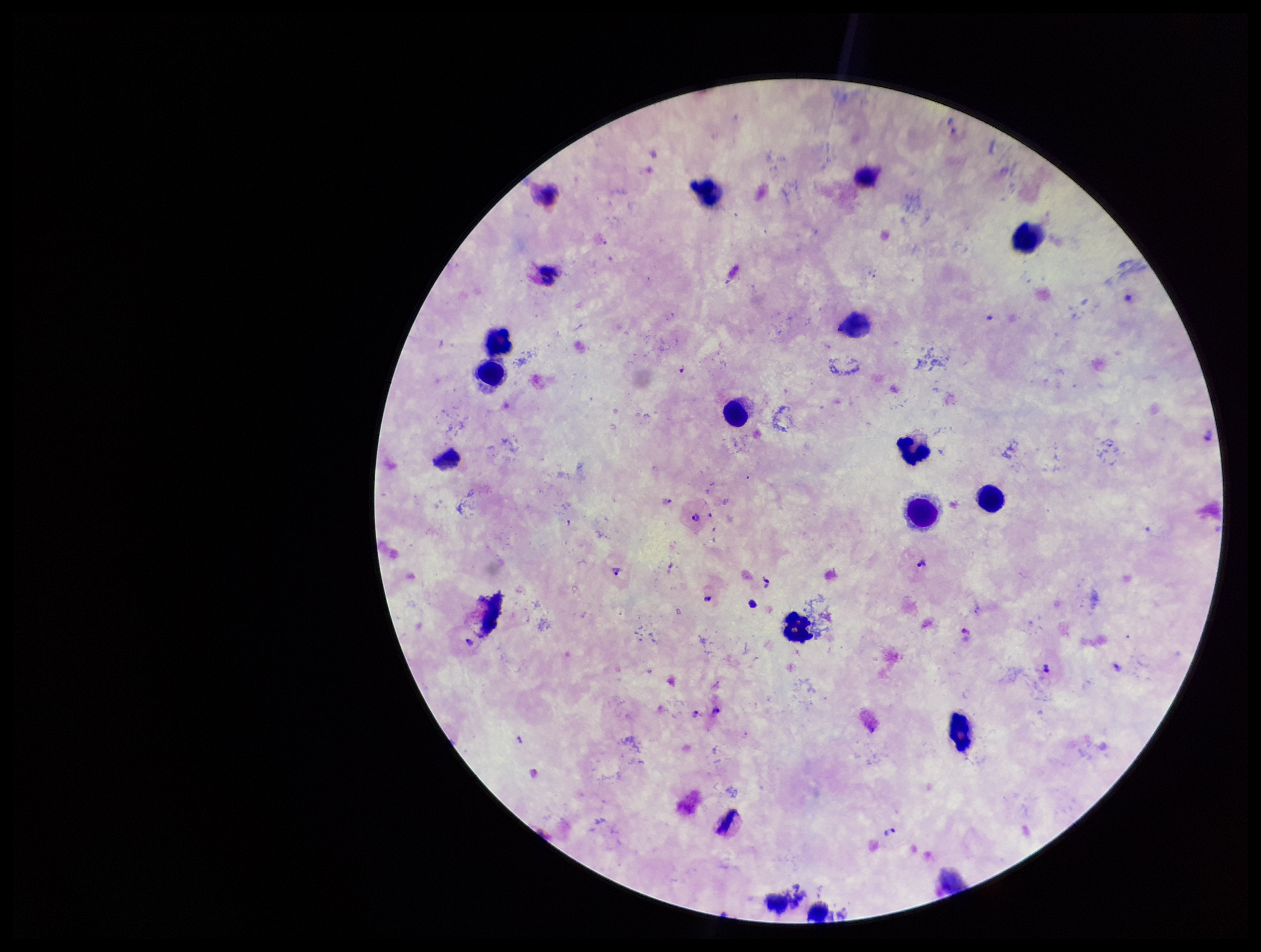

parasite count = 11
Plasmodium parasites = seen
preparation = thick
patient malaria status = infected
stain = Giemsa
capture = smartphone photograph through the microscope eyepiece
field of view = single
species reported for this patient = Plasmodium vivax
leukocyte count = 14
image size = 1261×952 pixels